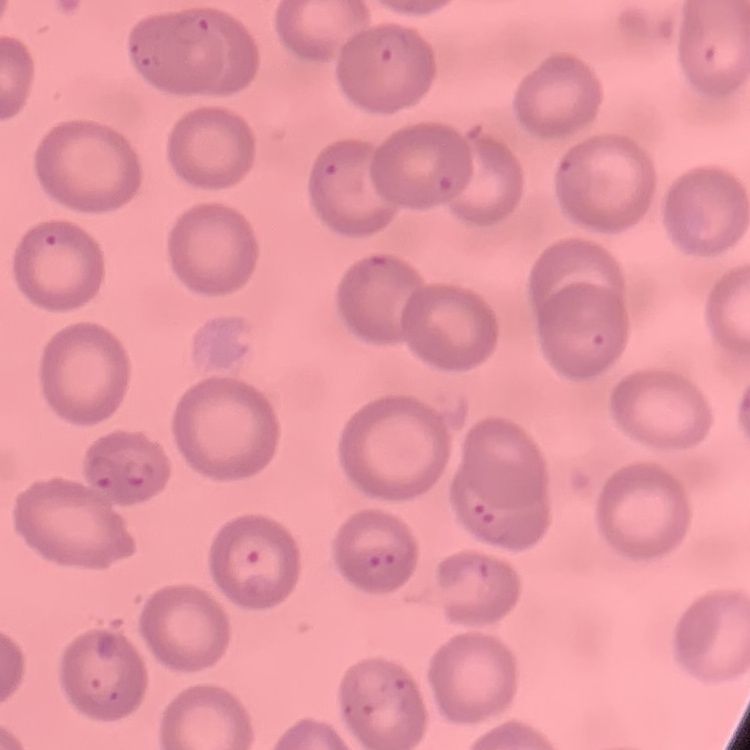
The erythrocytes exhibit no rouleaux formation. Stained with either Field's or Giemsa. Thin blood smear. One tile cut from a larger photomicrograph.